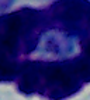
A white blood cell is seen. Photomicrograph. 1000x magnification.